Classify this cell by malaria status.
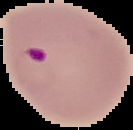
Parasitized.

image type = segmented cell region with the area outside set to black
image size = 133×130 pixels
preparation = thin blood film